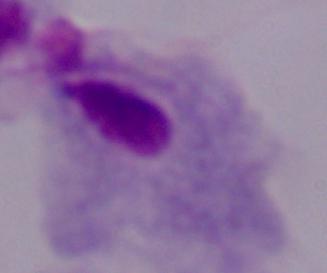

identification = trichomonad
magnification = 1000x
modality = photomicrograph